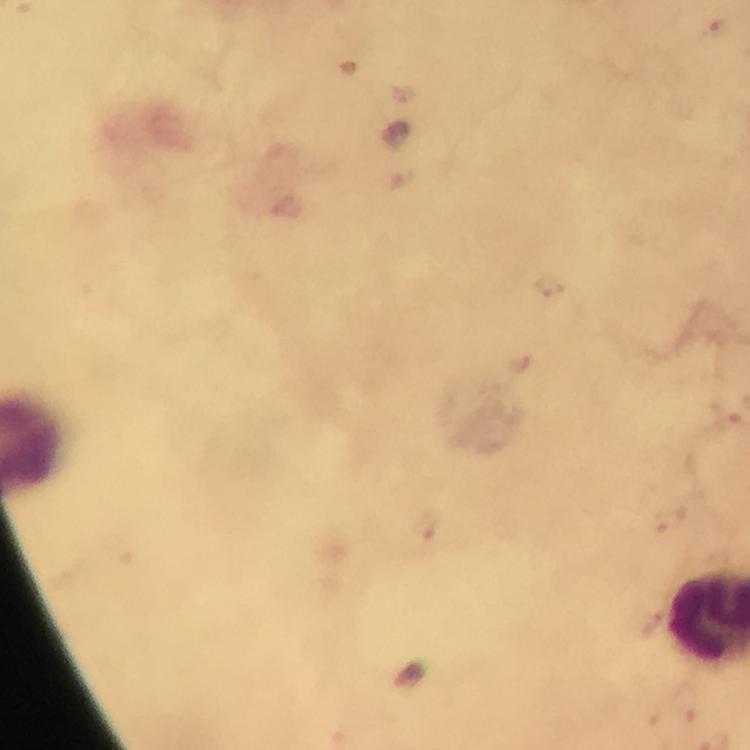

Approximate centers as {x, y} in pixels.
Summary:
  - Malaria parasite locations: {718, 32}, {400, 179}, {546, 286}, {424, 529}
  - Context: from a diagnostic examination for malaria
  - Immersion oil: used
  - Capture: smartphone camera through the microscope
  - Stain: Giemsa
  - Magnification: 100x
  - Preparation: thick smear
  - Image size: 750×750 pixels
  - Cropped from: one field of view